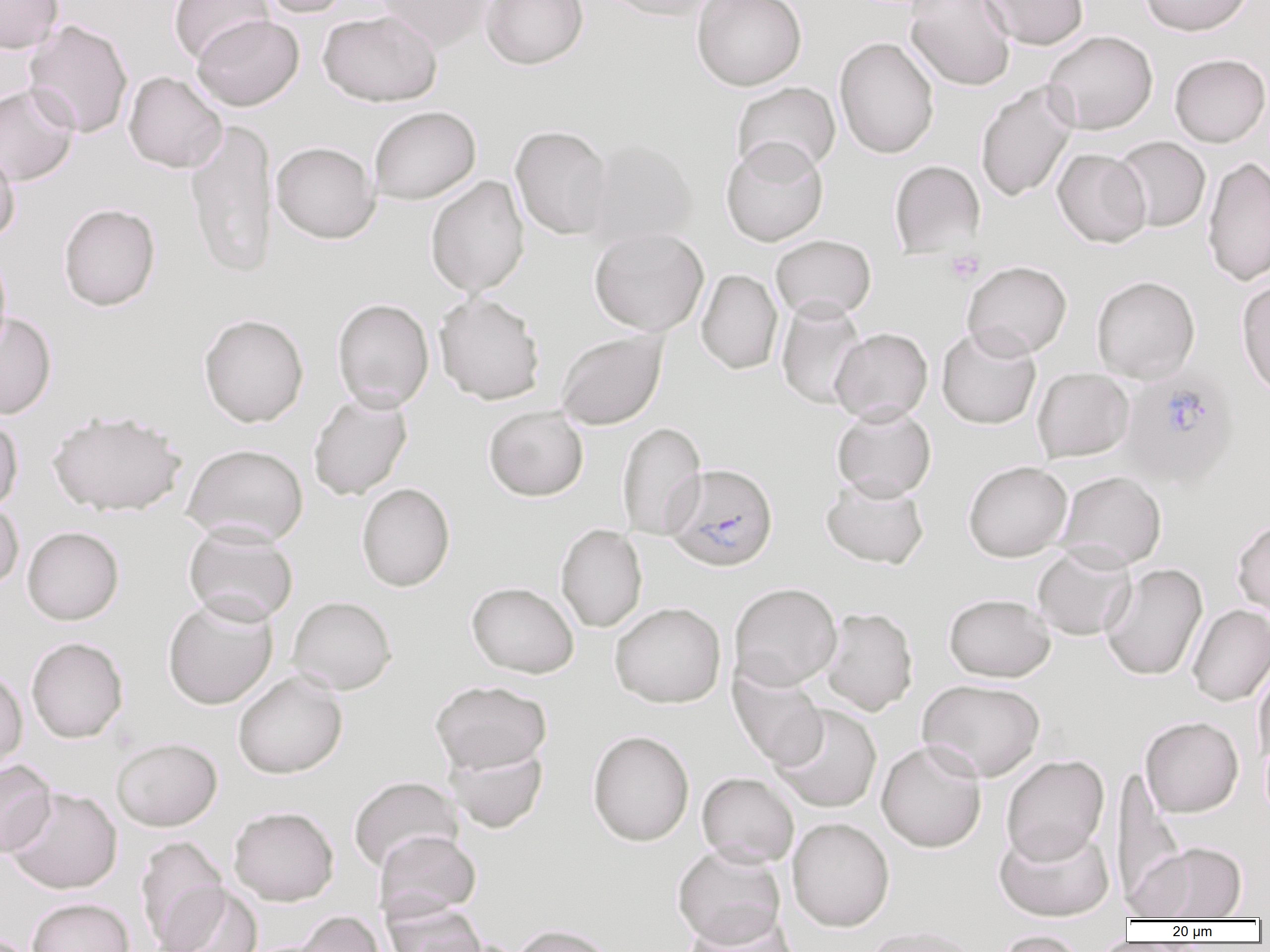
slide-level diagnosis = Plasmodium falciparum
preparation = thin blood film
field of view = single
Plasmodium falciparum-infected red blood cell locations = approximate bounding boxes as (x1,y1)-(x2,y2) corner pairs in pixels: (1120,369)-(1239,490), (665,463)-(778,571)
modality = optical microscopy
magnification = 1000x
platelet locations = approximate bounding boxes as (x1,y1)-(x2,y2) corner pairs in pixels: (945,250)-(984,284)
image size = 1270×952 pixels
uninfected red blood cell locations = approximate bounding boxes as (x1,y1)-(x2,y2) corner pairs in pixels: (0,0)-(64,53), (169,0)-(272,62), (256,0)-(353,18), (373,0)-(493,51), (481,0)-(588,69), (597,0)-(721,20), (691,0)-(807,91), (906,0)-(1016,91), (981,0)-(1088,50), (1139,0)-(1253,36), (318,10)-(441,106), (192,14)-(304,111), (23,19)-(133,138), (1042,30)-(1158,135), (834,36)-(939,159), (1169,53)-(1270,147), (123,71)-(227,173), (975,81)-(1078,202), (731,82)-(841,178), (0,84)-(80,186), (369,106)-(481,205), (185,117)-(279,279), (510,125)-(614,240), (1113,136)-(1211,232), (720,138)-(829,247), (585,139)-(698,246), (271,141)-(380,243), (0,144)-(21,245), (1052,148)-(1151,248), (1202,155)-(1270,286), (889,160)-(985,259), (425,176)-(530,297), (58,203)-(160,311), (589,227)-(709,336), (770,234)-(876,322), (0,247)-(12,358), (962,260)-(1072,359), (696,269)-(783,375), (1091,275)-(1200,383), (1236,278)-(1270,399), (434,292)-(546,405), (776,297)-(867,410), (332,298)-(434,412), (0,311)-(57,419), (199,313)-(309,427), (936,325)-(1041,429), (830,327)-(933,423), (556,330)-(668,430), (1032,368)-(1134,462), (308,392)-(412,501), (831,404)-(937,501), (483,406)-(589,501), (46,408)-(186,517), (0,414)-(23,515), (616,422)-(707,540), (182,443)-(309,546), (963,460)-(1072,562), (1054,470)-(1167,569), (821,476)-(929,569), (356,482)-(455,592), (0,500)-(23,591), (1232,516)-(1270,618), (556,523)-(647,633), (182,524)-(299,626), (22,526)-(124,625), (1032,545)-(1136,641), (1100,563)-(1208,681), (466,582)-(579,678), (729,582)-(842,690), (943,593)-(1055,682), (162,595)-(279,709), (287,595)-(397,695), (610,601)-(726,708), (1187,604)-(1270,707), (820,606)-(918,715), (26,637)-(128,743), (1253,662)-(1270,768), (728,665)-(828,770), (0,666)-(28,775), (232,670)-(348,779), (917,678)-(1045,782), (430,680)-(552,774), (770,704)-(883,814), (1140,716)-(1243,818), (587,730)-(694,846), (111,737)-(222,831), (876,740)-(987,853), (445,742)-(548,833), (1001,755)-(1110,865), (0,760)-(56,857), (1117,768)-(1185,908), (697,772)-(800,868), (348,776)-(464,874), (3,787)-(122,894), (229,806)-(339,906), (787,817)-(894,931), (994,823)-(1114,921), (373,830)-(481,922), (135,835)-(229,951), (1134,842)-(1247,920), (672,844)-(786,948), (154,884)-(263,952), (27,898)-(134,952), (383,900)-(487,952), (682,908)-(799,952), (289,910)-(387,952), (510,924)-(617,952), (861,925)-(981,952), (993,930)-(1087,952), (1093,932)-(1125,952)